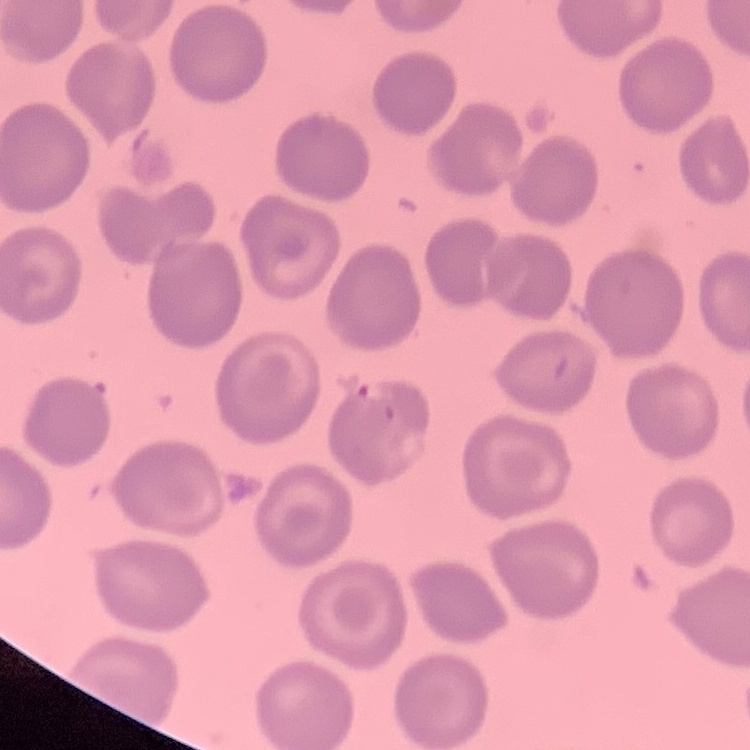

{
  "erythrocyte_morphology": "no rouleaux formation",
  "preparation": "thin blood film",
  "image_type": "square crop of a larger photomicrograph",
  "stain": "Field's or Giemsa"
}